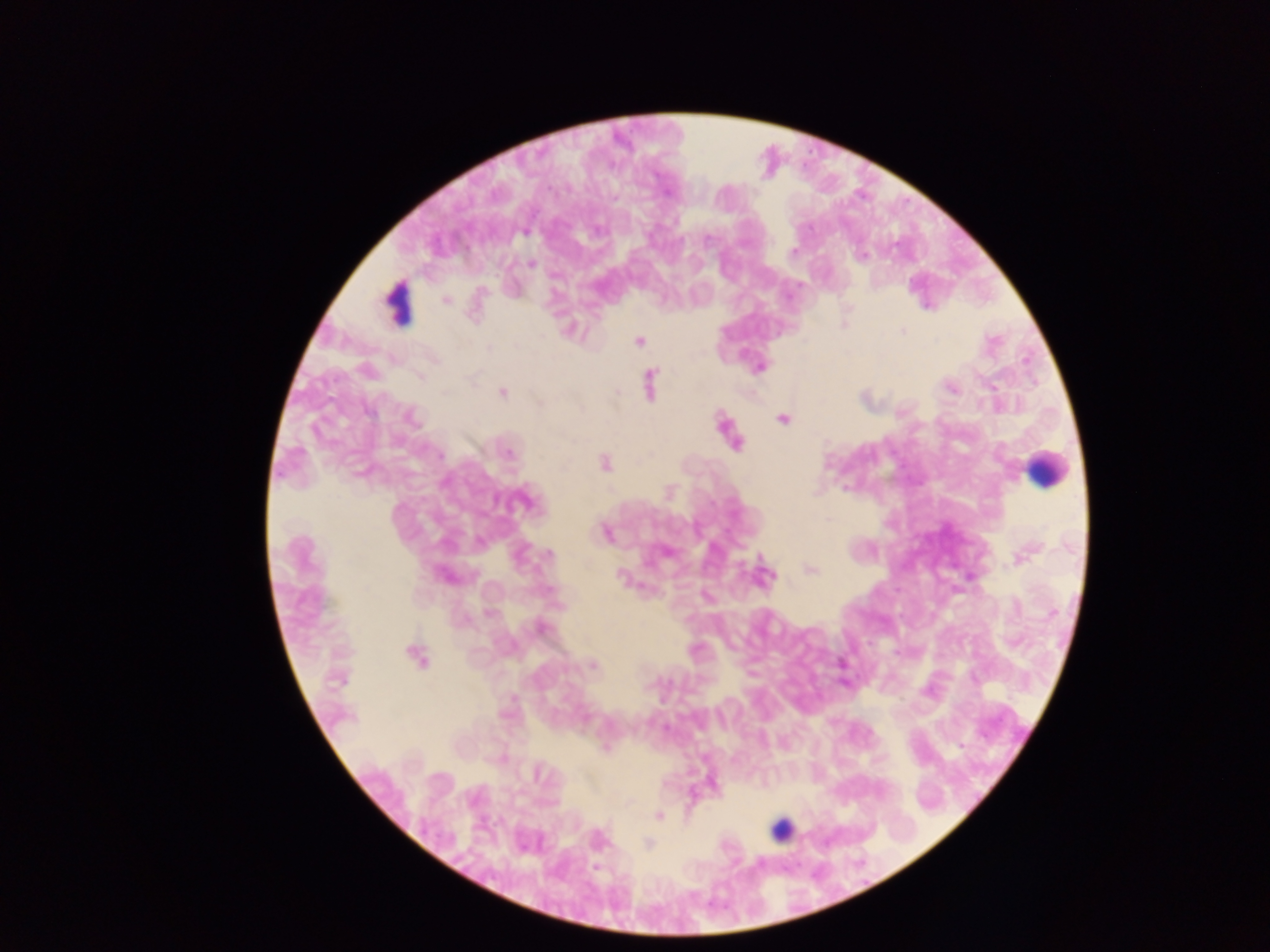

Approximate centers as [x, y] in pixels.
Summary:
  - Malaria parasite locations: [525, 232], [793, 252], [861, 256], [531, 264], [446, 300], [902, 331], [638, 342], [489, 348], [760, 367], [367, 370], [649, 384], [951, 389], [617, 391], [503, 393], [539, 403], [370, 412], [411, 418], [782, 419], [735, 442], [508, 453], [439, 455], [605, 464], [524, 501], [605, 533], [549, 555], [1022, 556], [810, 570], [444, 575], [766, 575], [621, 576], [541, 627], [417, 655], [593, 665], [960, 745], [606, 748], [537, 773], [659, 816], [599, 840], [648, 843]
  - Leukocyte locations: [399, 303], [1045, 469], [780, 829]
  - Capture: mobile-phone photograph through a microscope
  - Preparation: thick blood smear
  - Field of view: single
  - Image size: 1270×952 pixels
  - Country: Ghana